Identify the preparation type.
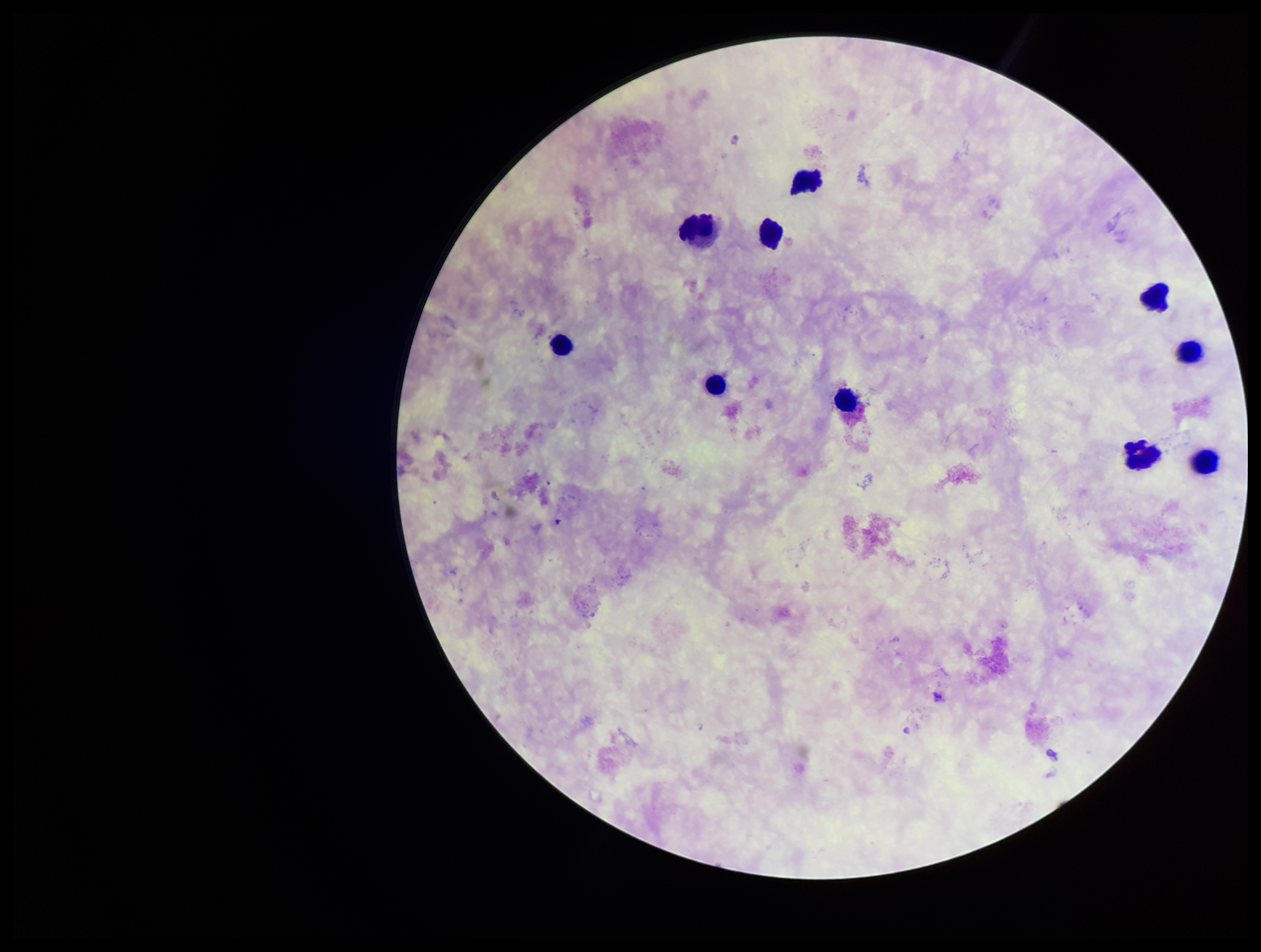
Thick.

Leukocyte count: 10. Stained with Giemsa. One field from this slide. Patient malaria status: negative. Photographed through the microscope eyepiece with a smartphone camera. Parasite count: 0. Image is 1261×952 pixels. Plasmodium parasites: none detected.